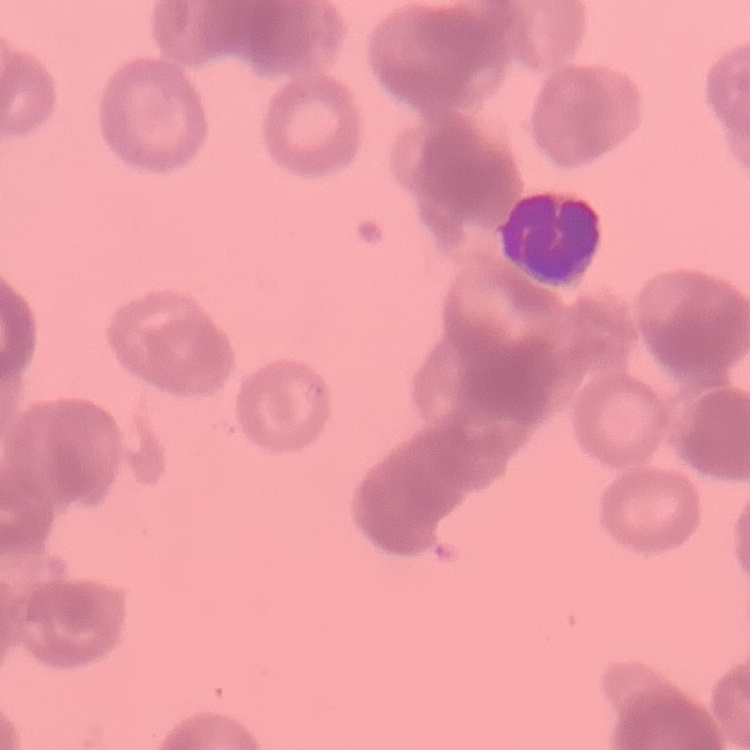

red blood cell morphology = rouleaux formation
image type = square crop of a larger photomicrograph
stain = Field's or Giemsa
preparation = thin peripheral smear